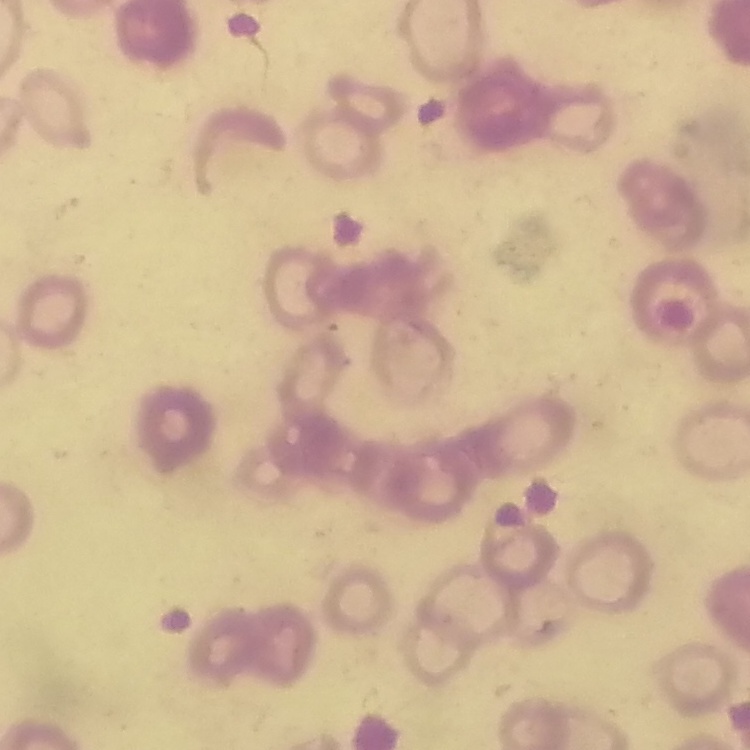
Summary:
  - Red blood cell morphology: rouleaux formation
  - Stain: Field's or Giemsa
  - Preparation: thin blood smear
  - Image type: square crop of a larger photomicrograph